Name the parasite shown.
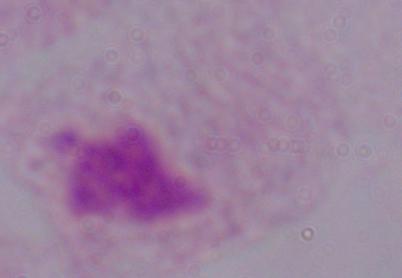

A trichomonad.

1000x magnification. Photomicrograph.